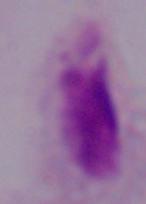

magnification = 1000x
identification = trichomonad
modality = micrograph